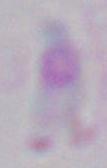

Summary:
  - Modality: photomicrograph
  - Magnification: 1000x
  - Identification: Toxoplasma gondii